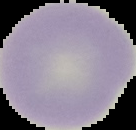
Result: no malaria parasites detected. Cell region segmented out of the field of view; the surrounding area is masked to black. From a thin blood smear. Image is 136×130 pixels.